Comment on the morphology of the red blood cells.
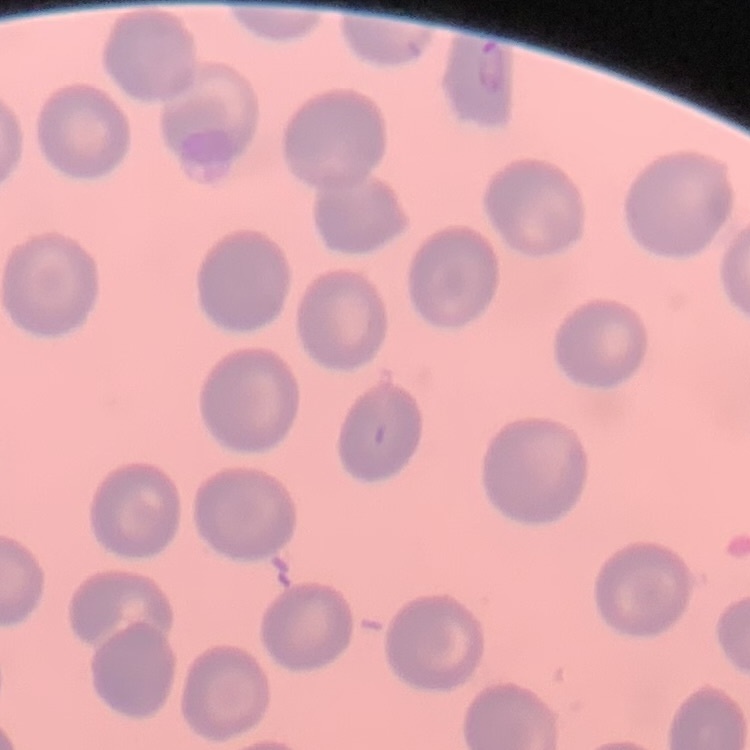
They show no rouleaux formation.

Summary:
  - Preparation: thin blood film
  - Stain: Field's or Giemsa
  - Image type: one tile cut from a larger photomicrograph